Classify this cell by malaria status.
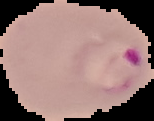
It is parasitized.

{
  "image_type": "segmented cell region with the area outside set to black",
  "preparation": "thin blood film",
  "image_size": "154×121 pixels"
}